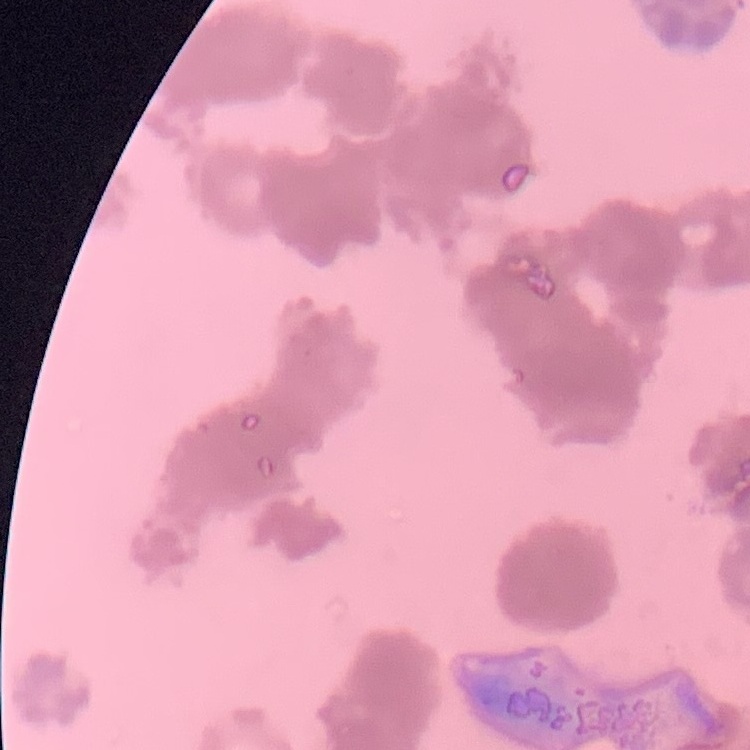
red blood cell morphology = rouleaux formation
image type = one tile cut from a larger photomicrograph
preparation = thin blood smear
stain = Field's or Giemsa